Classify this cell by malaria status.
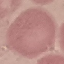

It is uninfected.

image_type: automatically extracted cell patch, resized to 64 × 64 pixels
stain: Giemsa
preparation: thin blood smear
capture: smartphone through the microscope eyepiece